Assess this cell for malaria.
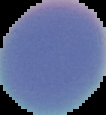

It is uninfected.

image type = cell region segmented out of the field of view; surrounding area masked to black
preparation = thin blood film
image size = 106×115 pixels